Classify this cell by malaria status.
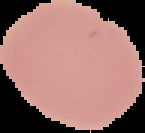
Uninfected.

Summary:
  - Image size: 145×133 pixels
  - Image type: segmented cell region on a black background
  - Preparation: thin blood film